Assess the morphology of the erythrocytes.
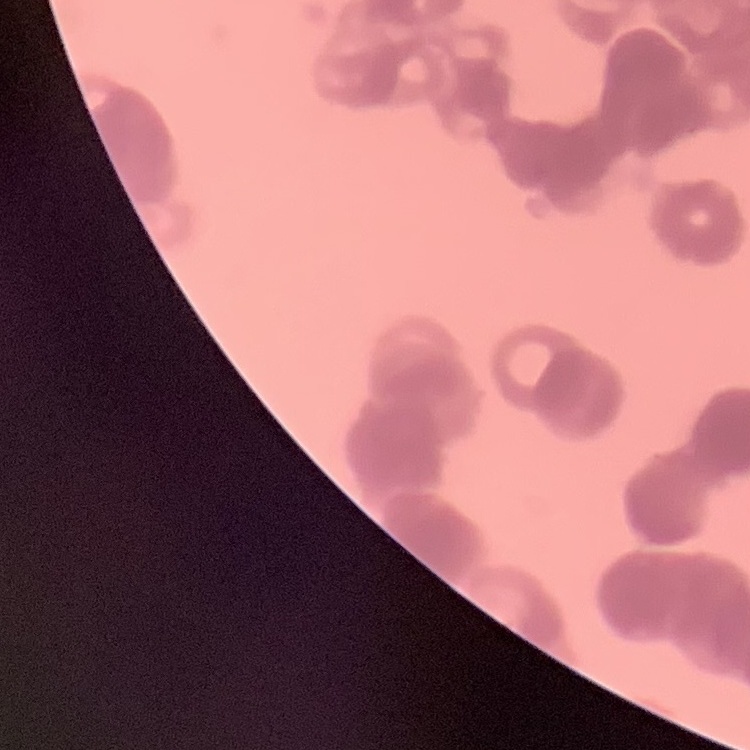
They show rouleaux formation.

stain = Field's or Giemsa
preparation = thin blood smear
image type = one tile cut from a larger photomicrograph